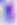
Summary:
  - Identification: Toxoplasma gondii
  - Magnification: 400x
  - Modality: photomicrograph